Assess this cell for malaria.
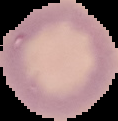
Uninfected.

Summary:
  - Image size: 118×121 pixels
  - Preparation: thin blood smear
  - Image type: segmented cell region with the area outside set to black